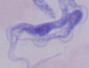

modality = photomicrograph
identification = trypanosome
magnification = 1000x